Identify the parasite.
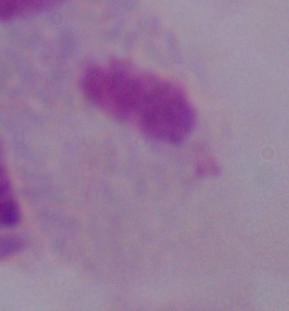

A trichomonad.

magnification: 1000x
modality: micrograph